Name the cell type shown.
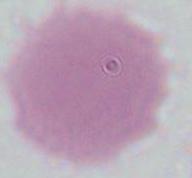

An erythrocyte.

Summary:
  - Magnification: 1000x
  - Modality: photomicrograph